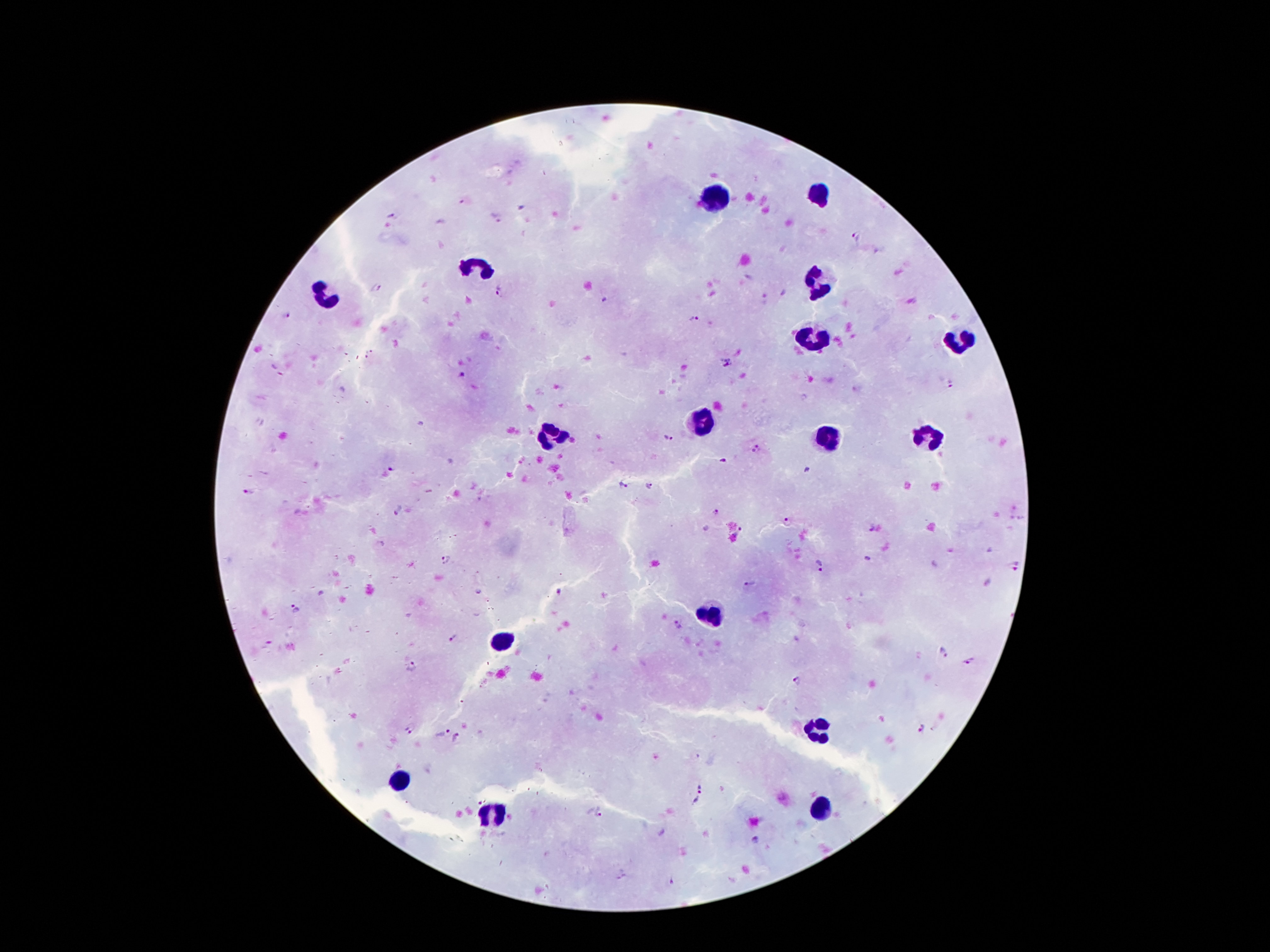 Approximate centers as (x, y) in pixels. Leukocyte locations: (712, 193), (820, 197), (480, 266), (819, 278), (325, 296), (810, 340), (956, 344), (702, 421), (927, 437), (551, 438), (827, 441), (714, 617), (503, 644), (819, 730), (399, 780), (822, 807), (490, 815). Malaria parasite locations: (462, 203), (391, 215), (497, 218), (857, 237), (376, 287), (500, 291), (286, 314), (691, 317), (727, 361), (462, 376), (951, 384), (670, 437), (756, 448), (723, 461), (393, 467), (624, 485), (649, 487), (248, 491), (398, 509), (716, 512), (790, 521), (871, 527), (739, 532), (446, 559), (820, 566), (1015, 566), (749, 583), (560, 590), (295, 607), (677, 623), (453, 636), (941, 653), (968, 661), (411, 666), (796, 682), (920, 728), (408, 730), (441, 731), (457, 738), (703, 791), (601, 814), (756, 840), (672, 882). 100x magnification. Patient malaria status: infected with Plasmodium falciparum. Giemsa-stained preparation. Image is 1270×952 pixels. One field from this slide. Photographed through the microscope eyepiece with a smartphone camera. Thick peripheral-blood smear.